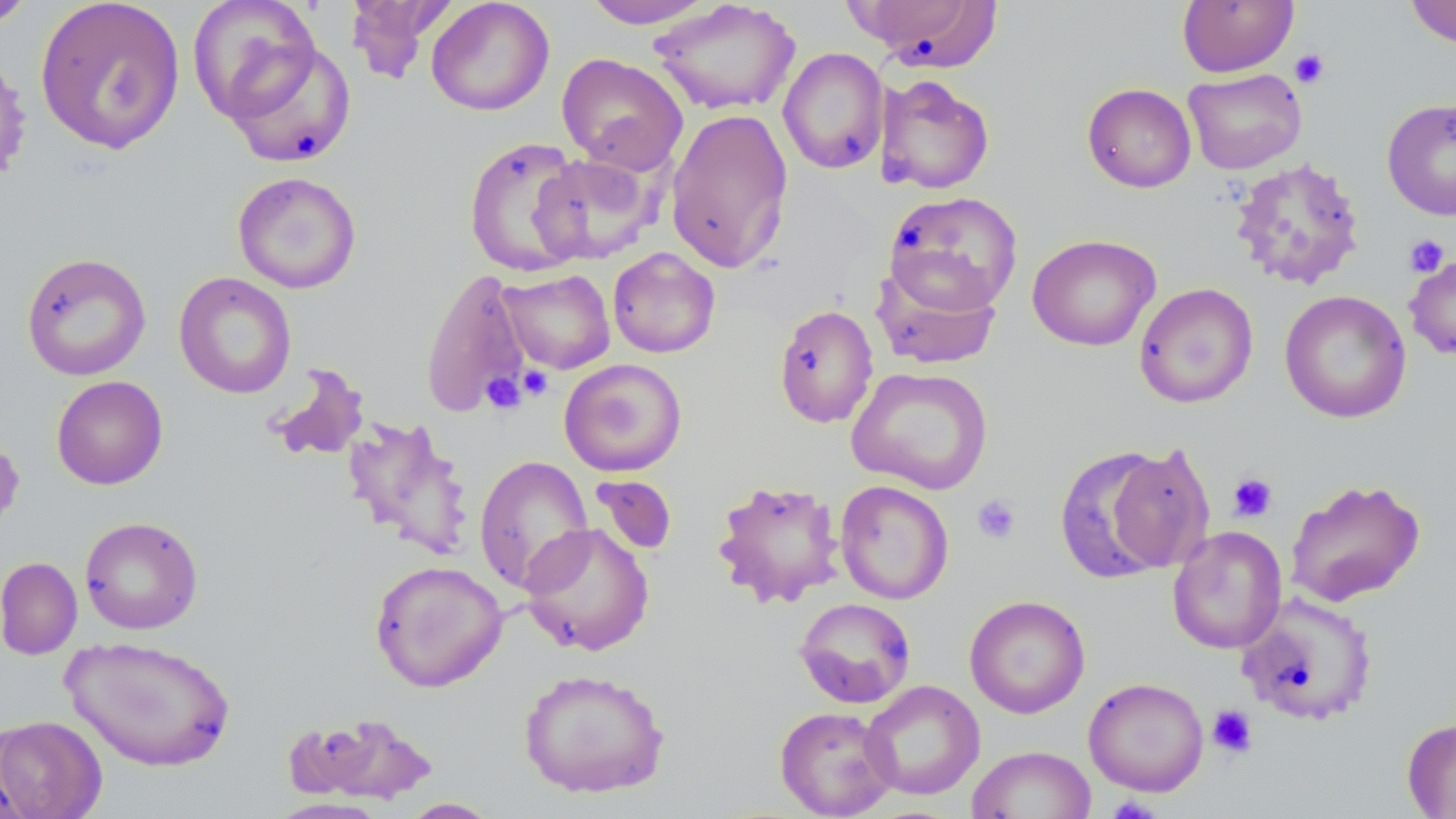
Summary:
  - Coordinate format: approximate bounding boxes as (x1,y1)-(x2,y2) corner pairs in pixels
  - Platelet locations: (1290,49)-(1330,88), (1404,234)-(1450,277), (518,366)-(553,400), (482,372)-(526,415), (1228,472)-(1278,522), (972,494)-(1021,544), (1207,705)-(1257,758), (1106,797)-(1162,819)
  - Uninfected red blood cell locations: (35,0)-(185,155), (186,0)-(323,122), (344,0)-(451,84), (426,0)-(554,116), (582,0)-(716,29), (845,0)-(1005,71), (1177,0)-(1299,77), (1404,0)-(1456,49), (0,1)-(38,30), (648,1)-(802,116), (224,41)-(357,169), (0,45)-(32,188), (778,48)-(889,174), (556,52)-(689,174), (1183,68)-(1307,174), (875,74)-(995,195), (1082,83)-(1196,193), (1382,98)-(1456,221), (666,107)-(794,274), (463,136)-(589,276), (530,153)-(657,264), (1228,157)-(1366,291), (232,171)-(362,294), (884,190)-(1023,315), (1027,233)-(1161,351), (607,247)-(720,358), (1404,251)-(1456,361), (20,252)-(151,381), (873,264)-(1001,370), (420,267)-(532,418), (498,269)-(615,374), (174,271)-(296,399), (1134,283)-(1258,408), (1279,290)-(1412,424), (774,304)-(878,429), (558,358)-(687,476), (264,363)-(370,464), (846,366)-(993,494), (51,375)-(168,490), (342,416)-(475,559), (0,433)-(25,538), (1103,441)-(1217,574), (1053,445)-(1179,584), (473,455)-(594,595), (590,475)-(677,556), (1285,477)-(1426,607), (713,479)-(845,608), (834,480)-(954,604), (79,516)-(203,634), (519,522)-(655,656), (1167,525)-(1287,654), (0,557)-(83,660), (369,559)-(508,693), (1236,592)-(1378,728), (964,595)-(1090,718), (794,597)-(916,708), (62,636)-(236,772), (518,668)-(671,799), (1083,677)-(1209,796), (860,680)-(984,800), (774,705)-(897,818), (290,711)-(439,806), (0,715)-(107,819), (1401,717)-(1456,818), (966,745)-(1097,819), (399,797)-(500,818)
  - Slide-level diagnosis: no evidence of blood parasites
  - Stain: May-Grünwald-Giemsa
  - Field of view: one of a larger specimen
  - Modality: optical microscopy
  - Magnification: 1000x
  - Preparation: thin blood smear
  - Image size: 1456×819 pixels